Assess the morphology of the erythrocytes.
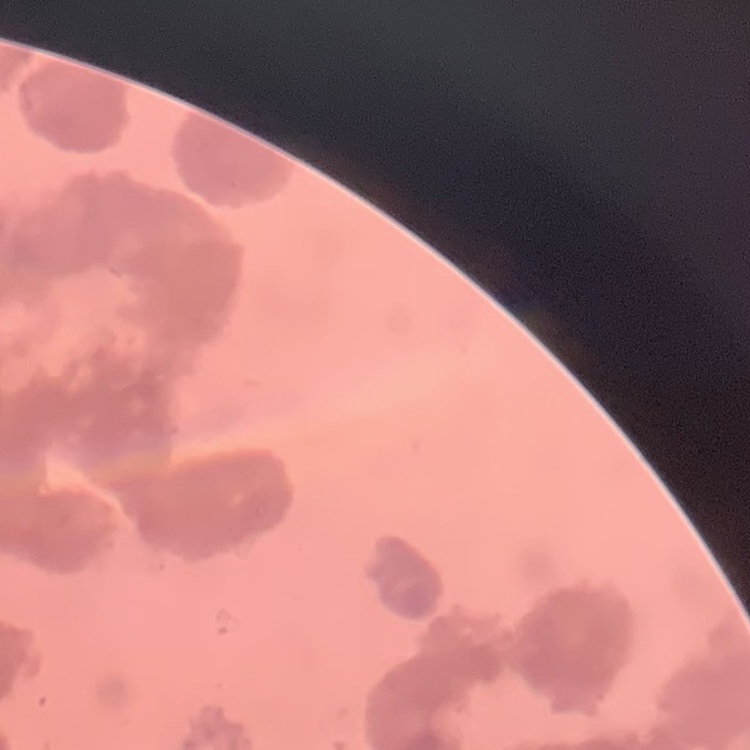
Rouleaux formation.

preparation = thin peripheral smear
image type = square crop of a larger photomicrograph
stain = Field's or Giemsa